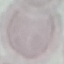

result = no malaria parasites seen
capture = smartphone camera at the microscope eyepiece
stain = Giemsa
preparation = thin smear
image type = automatically extracted cell patch, resized to 64 × 64 pixels